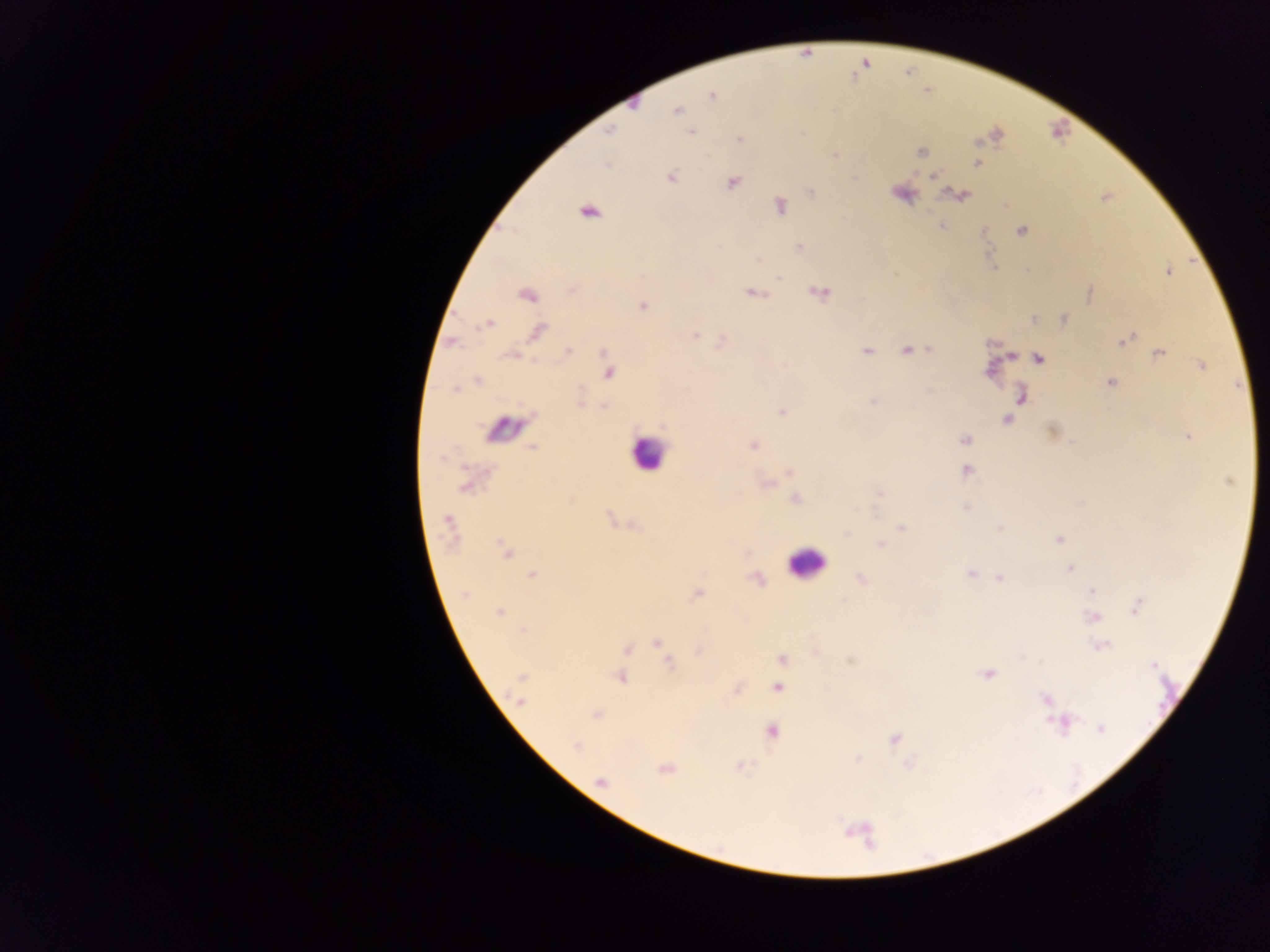

Approximate centers as {x, y} in pixels.
Summary:
  - Leukocyte locations: {646, 453}, {804, 563}
  - Plasmodium parasite locations: {712, 96}, {677, 110}, {609, 131}, {691, 131}, {739, 139}, {920, 152}, {977, 163}, {934, 176}, {671, 177}, {731, 183}, {811, 192}, {959, 195}, {780, 206}, {589, 212}, {1020, 231}, {799, 247}, {1168, 272}, {778, 278}, {753, 293}, {821, 293}, {1090, 293}, {527, 295}, {642, 306}, {1035, 319}, {1064, 319}, {488, 324}, {538, 332}, {695, 334}, {1125, 340}, {929, 349}, {907, 350}, {867, 351}, {567, 353}, {1157, 353}, {1011, 356}, {1039, 358}, {1202, 366}, {608, 372}, {478, 381}, {1111, 383}, {454, 389}, {581, 400}, {872, 402}, {604, 407}, {781, 412}, {1007, 419}, {1052, 430}, {1188, 437}, {965, 439}, {753, 445}, {533, 448}, {966, 471}, {789, 472}, {1229, 481}, {465, 486}, {879, 493}, {796, 498}, {965, 508}, {448, 522}, {902, 528}, {1000, 528}, {846, 533}, {1059, 539}, {880, 545}, {505, 550}, {1070, 570}, {971, 574}, {533, 576}, {861, 578}, {999, 578}, {1092, 590}, {465, 594}, {698, 594}, {1138, 606}, {499, 612}, {1092, 617}, {657, 642}, {1102, 645}, {627, 650}, {700, 651}, {782, 659}, {670, 663}, {1153, 666}, {988, 674}, {523, 676}, {621, 678}, {777, 688}, {1045, 699}, {521, 702}, {596, 715}, {1063, 724}, {1100, 728}, {772, 731}, {894, 739}, {575, 746}, {857, 759}, {664, 768}, {602, 782}
  - Country: Ghana
  - Field of view: single
  - Capture: mobile-phone photograph through a microscope
  - Image size: 1270×952 pixels
  - Preparation: thick blood smear